Assess this cell for malaria.
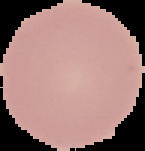

Uninfected.

Image is 145×151 pixels. From a thin blood smear. Segmented cell region on a black background.